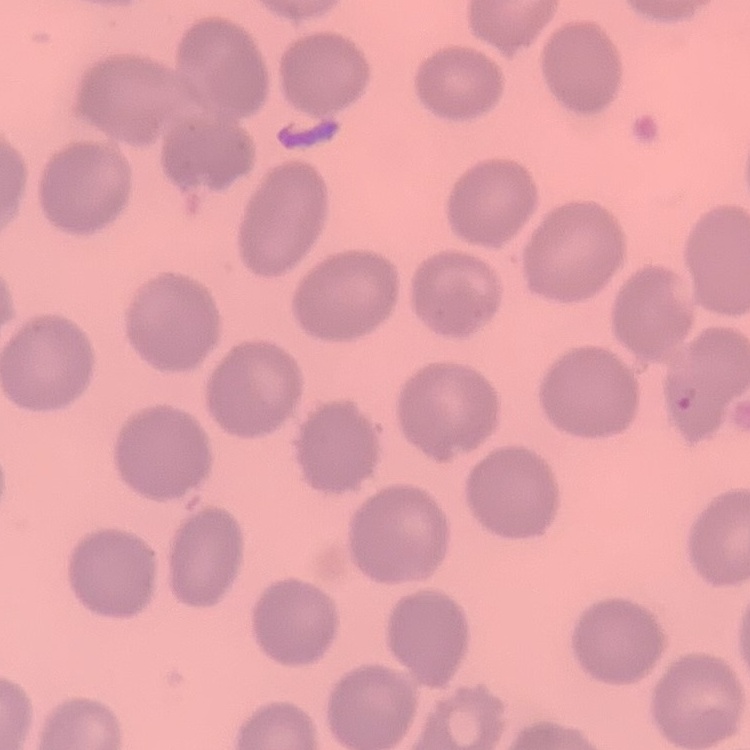 The red blood cells show no rouleaux formation. Stained with either Field's or Giemsa. Thin blood smear. Square crop of a larger photomicrograph.